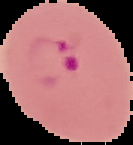
From a thin blood smear. Result: Plasmodium parasites identified. Segmented cell region on a black background. Image is 133×145 pixels.